Locate platelets.
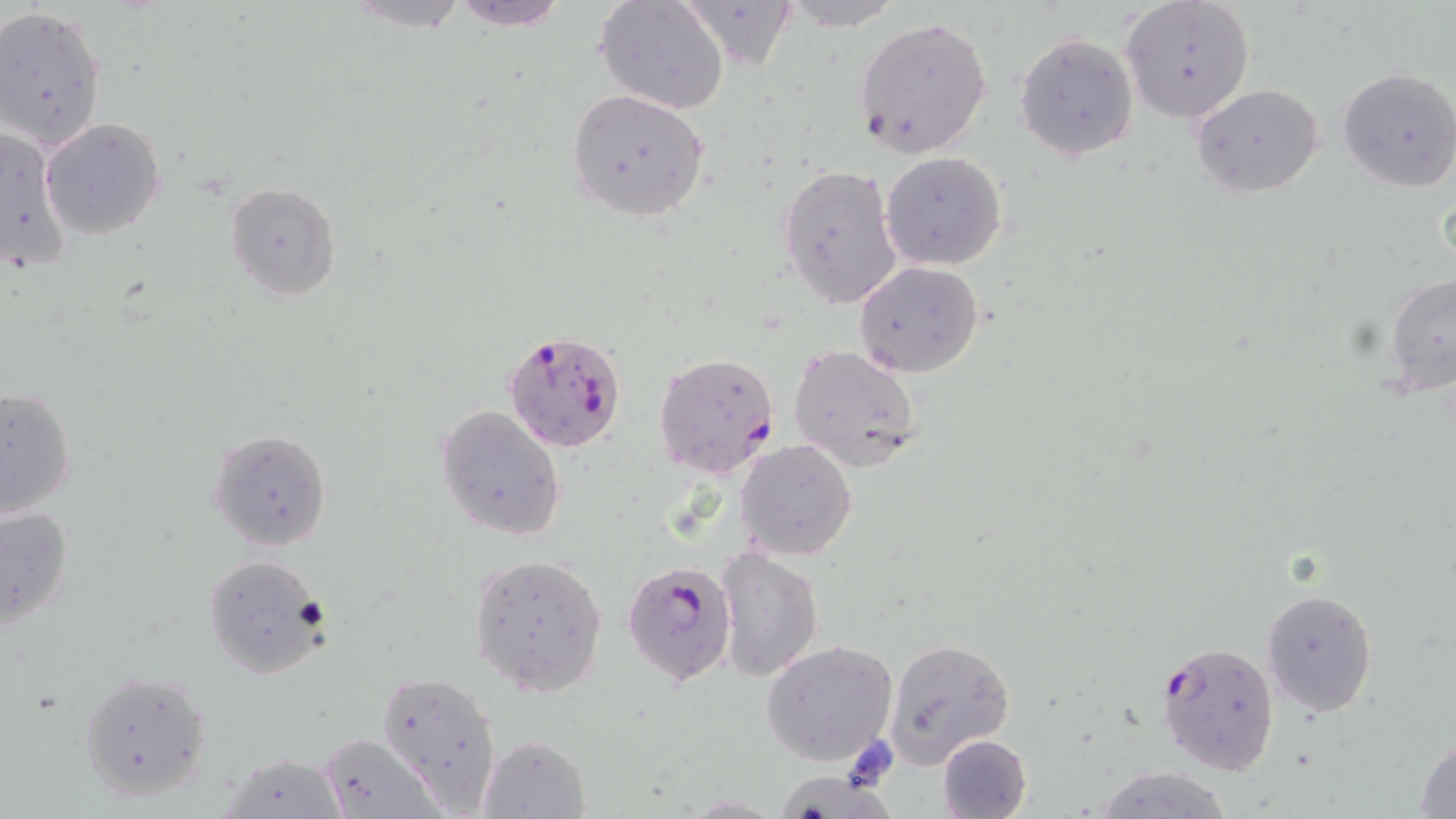
Approximate bounding boxes as (x1, y1, x2, y2) in pixels.
Platelets: (842, 737, 897, 788).

Uninfected red blood cell locations: (338, 0, 475, 33), (448, 0, 568, 30), (594, 0, 732, 115), (781, 0, 906, 30), (1120, 0, 1254, 124), (674, 1, 798, 68), (0, 6, 107, 149), (852, 16, 993, 159), (1014, 33, 1138, 162), (1336, 66, 1456, 194), (1192, 83, 1325, 198), (566, 88, 709, 220), (40, 118, 167, 240), (0, 124, 74, 276), (880, 152, 1007, 271), (777, 162, 904, 311), (225, 182, 340, 301), (853, 260, 985, 379), (1382, 270, 1456, 400), (788, 344, 923, 472), (0, 384, 77, 520), (435, 403, 566, 541), (208, 428, 334, 552), (735, 438, 858, 560), (1, 505, 74, 635), (714, 547, 824, 682), (469, 553, 608, 698), (202, 554, 328, 678), (1261, 588, 1378, 716), (883, 638, 1015, 765), (759, 641, 900, 765), (79, 670, 212, 803), (378, 670, 502, 811), (318, 732, 443, 817), (936, 733, 1033, 818), (478, 735, 590, 817), (1413, 739, 1456, 818), (217, 751, 348, 817), (1092, 766, 1235, 819), (764, 769, 899, 819). Plasmodium falciparum-infected red blood cell locations: (504, 328, 629, 457), (652, 352, 780, 479), (622, 559, 735, 685), (1156, 640, 1281, 777). Slide-level diagnosis: Plasmodium falciparum. Captured at 1000x magnification. Optical microscopy. May-Grünwald-Giemsa stain. Image is 1456×819 pixels. Thin blood film. Single field of view.